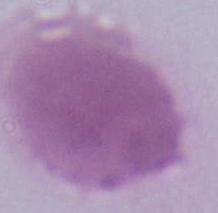

Summary:
  - Magnification: 1000x
  - Identification: erythrocyte
  - Modality: photomicrograph